Give the position of every Plasmodium parasite.
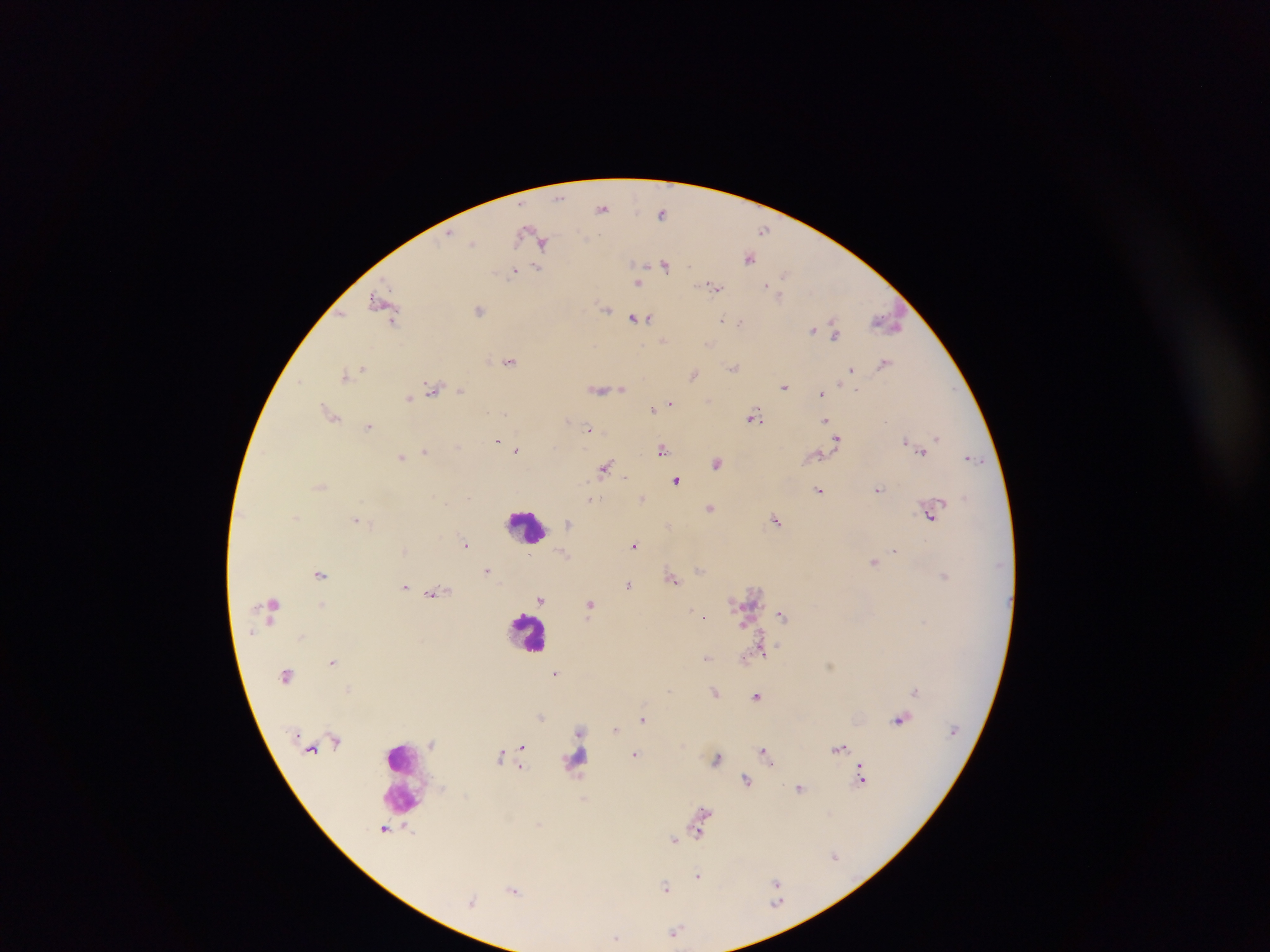

Approximate centers as x y in pixels.
Plasmodium parasites: 560 198; 602 208; 662 212; 525 230; 764 231; 473 242; 543 242; 749 258; 665 265; 538 268; 513 272; 784 274; 639 283; 767 285; 713 286; 778 296; 382 303; 605 309; 479 310; 634 318; 722 319; 392 321; 740 321; 887 322; 813 329; 835 334; 662 341; 709 345; 510 362; 885 363; 734 367; 363 368; 850 370; 345 374; 693 375; 301 380; 784 387; 433 388; 621 389; 856 389; 460 390; 600 390; 821 393; 409 398; 670 403; 652 409; 329 412; 755 416; 825 421; 369 426; 589 429; 937 437; 497 440; 836 440; 905 440; 458 446; 518 449; 662 450; 425 452; 922 452; 402 456; 972 459; 717 463; 604 468; 626 478; 676 479; 319 486; 878 489; 819 490; 469 497; 643 497; 589 499; 711 507; 930 514; 355 518; 776 520; 568 523; 466 544; 635 545; 896 550; 529 555; 874 561; 487 570; 700 570; 321 574; 945 576; 673 578; 629 584; 404 586; 436 592; 540 600; 323 604; 590 604; 273 605; 782 615; 704 617; 251 632; 302 637; 761 646; 706 657; 332 661; 555 674; 915 691; 715 693; 757 696; 541 717; 643 719; 899 719; 616 729; 580 731; 523 747; 839 748; 766 752; 636 754; 500 756; 718 758; 861 776; 746 780; 800 789; 702 816; 385 829; 700 829; 409 831; 674 839; 834 856; 698 875; 776 884; 665 886; 514 890; 776 892; 472 901; 675 932; 616 938.

Summary:
  - Leukocyte locations: 527 526; 528 632; 401 776
  - Image size: 1270×952 pixels
  - Preparation: thick blood film
  - Capture: mobile-phone photograph through a microscope
  - Field of view: single
  - Country: Ghana